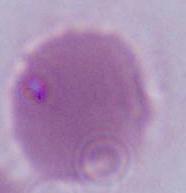

A red blood cell is shown. Micrograph. 1000x magnification.